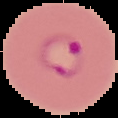
Summary:
  - Image size: 118×118 pixels
  - Image type: segmented cell region on a black background
  - Result: malaria parasites detected
  - Preparation: thin blood film